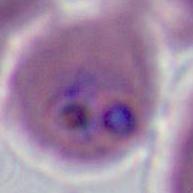 400x or 1000x magnification. Photomicrograph. A Plasmodium parasite is shown.